Give the position of every Plasmodium parasite and every leukocyte.
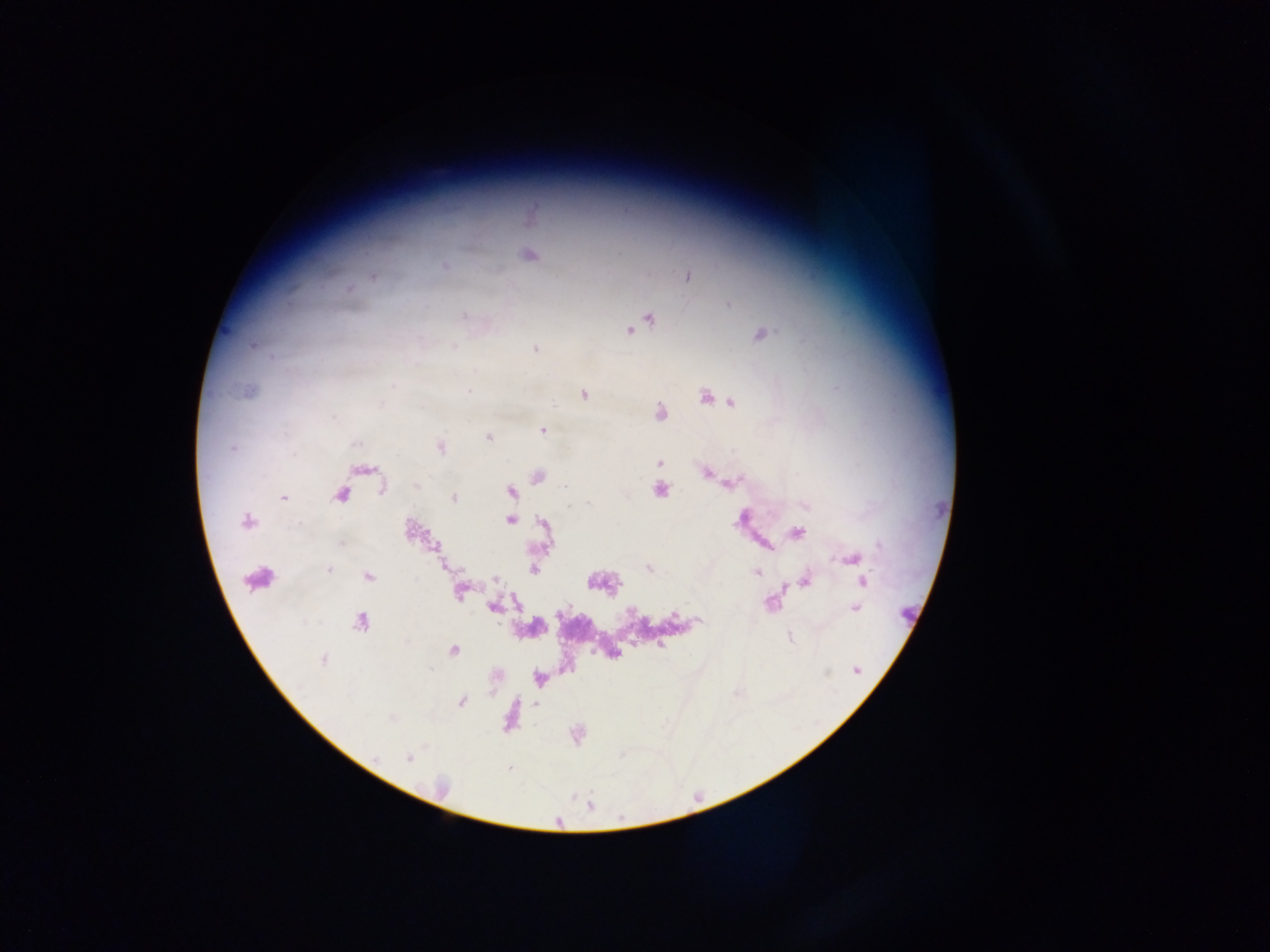
Approximate centers as x y in pixels.
Plasmodium parasites: 529 255; 445 266; 372 277; 688 277; 728 305; 464 316; 649 318; 642 323; 630 331; 762 334; 253 346; 454 347; 535 349; 392 385; 468 390; 248 391; 584 394; 704 398; 731 402; 659 413; 542 431; 489 437; 354 444; 232 447; 441 447; 659 463; 366 470; 706 473; 539 476; 731 483; 416 485; 567 486; 381 488; 660 489; 511 491; 341 496; 283 497; 453 498; 806 505; 510 520; 246 522; 412 530; 797 533; 341 544; 854 559; 649 569; 328 570; 534 570; 756 572; 368 577; 496 578; 806 580; 862 582; 460 592; 494 607; 854 608; 674 617; 699 621; 360 622; 789 637; 661 646; 453 651; 323 659; 856 670; 461 701; 535 704; 409 758; 508 768.
Leukocytes: 262 575.

Summary:
  - Country: Ghana
  - Preparation: thick blood smear
  - Capture: mobile-phone photograph through a microscope
  - Image size: 1270×952 pixels
  - Field of view: single